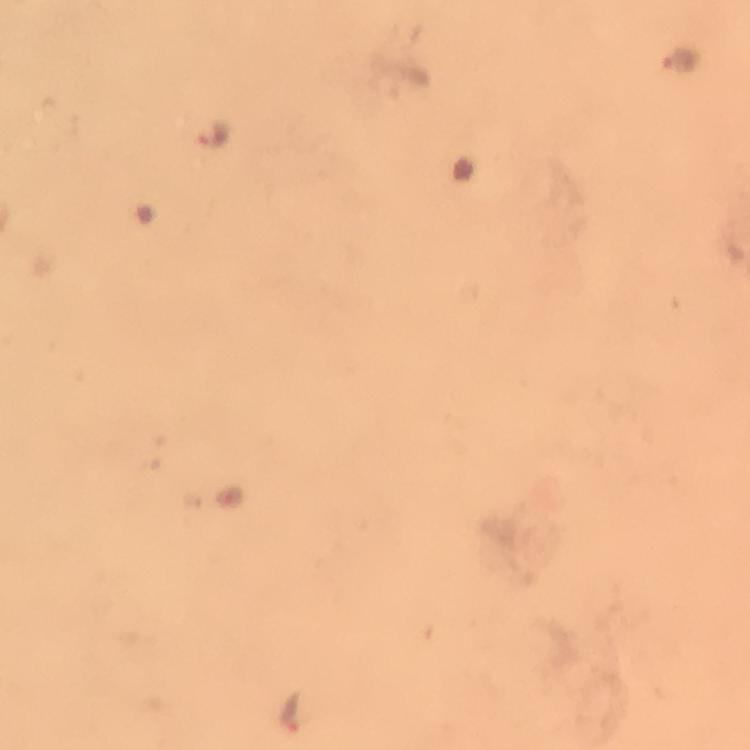 Approximate centers as {x, y} in pixels. Plasmodium parasite locations: {679, 58}, {213, 137}, {289, 711}. Immersion oil was used. Giemsa stain. Thick smear. Photographed through the microscope with a smartphone camera. A crop from one field of view. 100x magnification. From a malaria diagnostic workup. Image is 750×750 pixels.